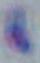
Summary:
  - Identification: Toxoplasma gondii
  - Magnification: 1000x
  - Modality: micrograph